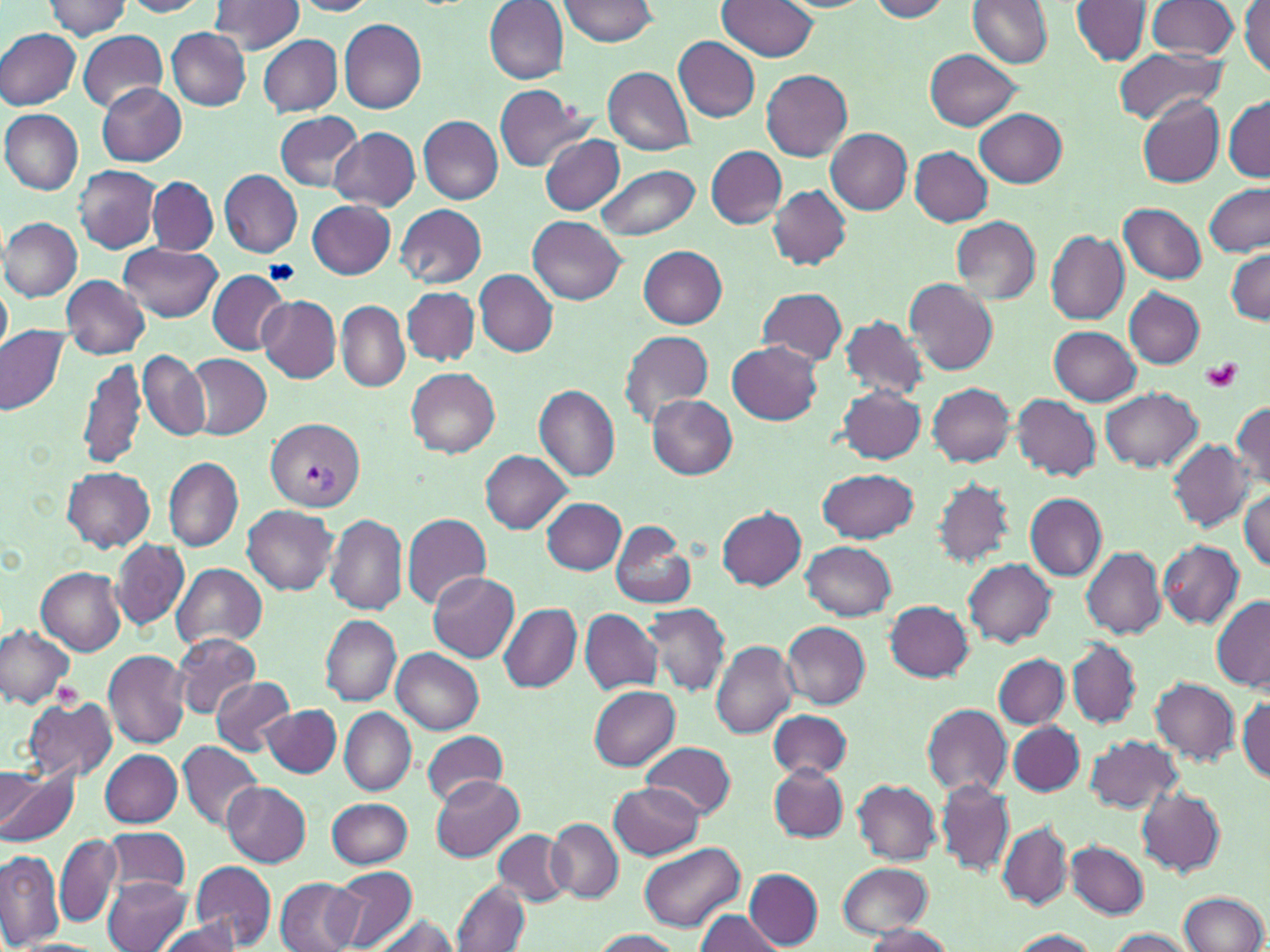

Approximate bounding boxes as [x1, y1, x2, y2] in pixels. Platelet locations: [1201, 359, 1243, 392]. Uninfected red blood cell locations: [43, 0, 133, 40], [119, 0, 213, 17], [208, 0, 304, 54], [557, 0, 661, 47], [719, 0, 821, 61], [867, 0, 953, 21], [969, 0, 1054, 68], [1071, 0, 1153, 66], [290, 1, 379, 17], [485, 1, 568, 84], [1241, 1, 1269, 77], [1145, 2, 1240, 60], [339, 18, 427, 114], [166, 27, 250, 111], [1, 28, 80, 109], [78, 30, 167, 112], [257, 35, 342, 117], [674, 37, 760, 122], [1112, 46, 1228, 124], [925, 50, 1022, 130], [602, 66, 694, 156], [761, 69, 853, 160], [96, 83, 185, 166], [492, 85, 591, 170], [1136, 94, 1224, 187], [1223, 95, 1270, 181], [975, 108, 1067, 189], [2, 110, 83, 195], [275, 111, 365, 193], [419, 116, 502, 203], [330, 127, 420, 211], [825, 128, 912, 214], [540, 133, 625, 215], [707, 146, 786, 228], [909, 147, 992, 225], [595, 164, 700, 243], [75, 165, 160, 252], [218, 169, 303, 258], [148, 176, 219, 255], [1205, 182, 1269, 257], [767, 186, 850, 270], [307, 200, 395, 279], [316, 200, 398, 361], [1119, 202, 1207, 284], [395, 203, 487, 288], [950, 216, 1040, 305], [2, 217, 82, 302], [529, 217, 625, 304], [1045, 230, 1129, 324], [118, 243, 221, 323], [638, 246, 728, 328], [1228, 249, 1270, 323], [208, 269, 289, 354], [474, 270, 557, 356], [61, 276, 150, 359], [903, 279, 999, 375], [0, 285, 11, 357], [403, 286, 480, 365], [1124, 287, 1205, 368], [758, 288, 850, 365], [256, 295, 342, 383], [1067, 295, 1210, 384], [337, 301, 407, 390], [839, 315, 928, 400], [0, 326, 68, 414], [1048, 326, 1141, 406], [619, 329, 714, 425], [726, 340, 824, 425], [138, 348, 210, 442], [188, 354, 272, 438], [77, 357, 147, 471], [406, 368, 500, 456], [929, 383, 1016, 466], [534, 384, 620, 482], [838, 384, 927, 463], [1101, 388, 1202, 470], [1010, 393, 1101, 481], [647, 395, 737, 479], [1232, 402, 1270, 487], [1168, 440, 1253, 530], [480, 451, 573, 532], [164, 456, 242, 551], [61, 466, 154, 551], [816, 468, 919, 544], [931, 478, 1014, 567], [1240, 488, 1270, 572], [1026, 493, 1108, 579], [541, 499, 626, 573], [243, 504, 339, 594], [718, 506, 807, 590], [326, 514, 407, 615], [401, 514, 492, 610], [610, 522, 695, 610], [111, 539, 188, 630], [1159, 540, 1243, 627], [802, 541, 896, 621], [1081, 546, 1166, 638], [964, 559, 1055, 647], [173, 563, 268, 650], [36, 568, 126, 655], [428, 571, 519, 660], [1212, 596, 1270, 690], [883, 600, 974, 682], [497, 603, 581, 692], [643, 603, 731, 695], [580, 608, 661, 694], [320, 615, 402, 706], [782, 621, 871, 708], [0, 625, 75, 709], [172, 632, 260, 717], [711, 640, 798, 737], [1067, 640, 1139, 727], [104, 649, 190, 750], [392, 649, 483, 734], [993, 654, 1068, 728], [211, 675, 294, 756], [1151, 678, 1239, 764], [589, 685, 681, 770], [21, 694, 118, 783], [1236, 696, 1269, 784], [920, 703, 1011, 799], [262, 704, 341, 778], [339, 707, 417, 795], [768, 710, 851, 779], [1008, 721, 1084, 795], [420, 730, 510, 805], [1086, 736, 1181, 813], [178, 741, 262, 831], [643, 741, 735, 821], [99, 749, 182, 827], [769, 763, 847, 841], [0, 765, 74, 846], [2, 768, 40, 838], [430, 776, 525, 861], [853, 778, 940, 864], [937, 780, 1014, 877], [221, 781, 312, 865], [610, 784, 704, 859], [1135, 787, 1225, 878], [326, 797, 413, 869], [950, 805, 1068, 900], [546, 818, 623, 902], [999, 823, 1071, 907], [99, 828, 192, 895], [494, 828, 573, 906], [54, 834, 123, 928], [637, 839, 745, 930], [1066, 840, 1148, 919], [0, 850, 62, 948], [190, 861, 277, 950], [837, 862, 934, 939], [331, 866, 417, 950], [744, 868, 823, 949], [104, 876, 190, 952], [275, 877, 363, 952], [452, 878, 528, 952], [1180, 891, 1267, 952], [694, 911, 784, 952], [365, 913, 464, 952], [156, 916, 241, 952], [860, 925, 954, 952], [1106, 927, 1200, 951], [1006, 928, 1100, 951], [591, 929, 684, 951], [11, 939, 102, 951]. Plasmodium vivax-infected red blood cell locations: [265, 418, 364, 514]. Slide-level diagnosis: Plasmodium vivax. Optical microscopy. Thin blood smear. Single field of view. Captured at 1000x magnification. May-Grünwald-Giemsa-stained preparation. Image is 1270×952 pixels.